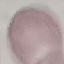

Malaria status: uninfected. Automatically extracted cell patch, resized to 64 × 64 pixels. Thin blood film. Giemsa stain. Acquired by smartphone through the microscope eyepiece.